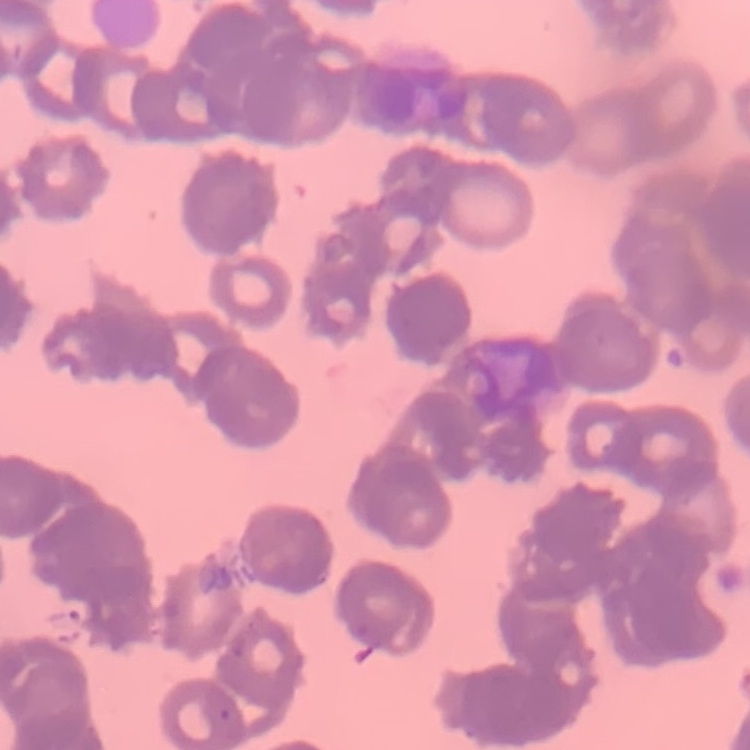

Summary:
  - Red blood cell morphology: rouleaux formation
  - Image type: square crop of a larger photomicrograph
  - Preparation: thin blood smear
  - Stain: Field's or Giemsa